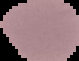

From a thin blood film. Malaria status: uninfected. Cell region segmented out of the field of view; the surrounding area is masked to black. Image is 79×61 pixels.